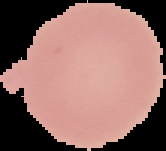

Summary:
  - Preparation: thin blood smear
  - Result: negative for malaria parasites
  - Image type: segmented cell region with the area outside set to black
  - Image size: 166×151 pixels